Give the position of every leukocyte visible.
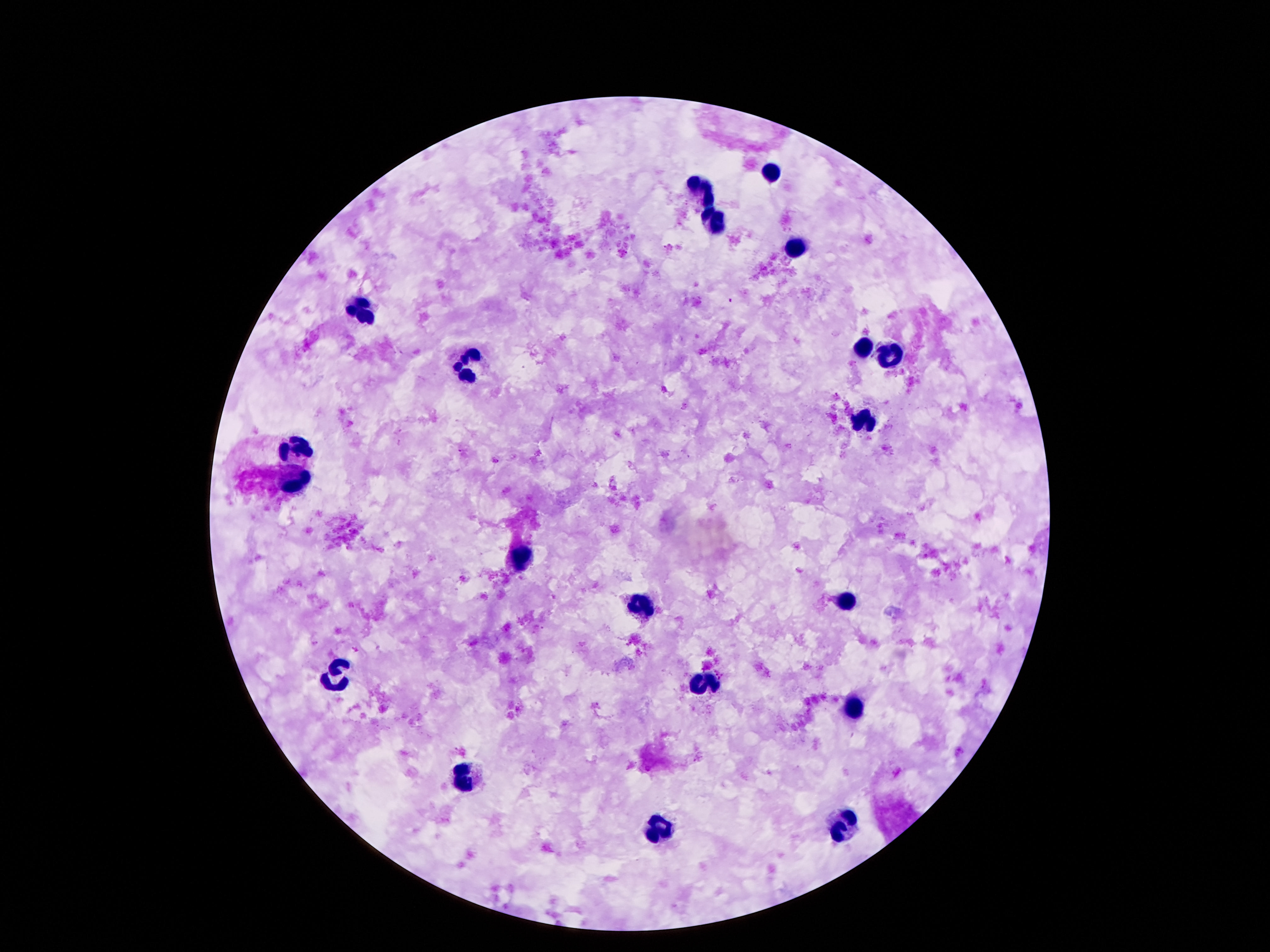

Approximate centers as {x, y} in pixels.
Leukocytes: {775, 172}, {705, 188}, {713, 224}, {797, 247}, {360, 310}, {862, 348}, {892, 354}, {470, 363}, {867, 420}, {297, 447}, {295, 482}, {521, 562}, {846, 598}, {643, 610}, {341, 678}, {705, 687}, {853, 708}, {465, 778}, {845, 827}, {657, 834}.

Patient malaria status: uninfected. Thick blood smear. Photographed through the microscope eyepiece with a smartphone camera. Single field of view. 100x magnification. Image is 1270×952 pixels. Giemsa-stained preparation.